Assess this cell for malaria.
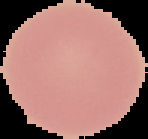
It is uninfected.

Summary:
  - Preparation: thin blood smear
  - Image type: segmented cell region on a black background
  - Image size: 148×139 pixels